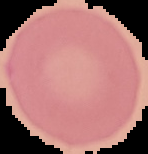
Image is 148×154 pixels. The area outside the segmented cell region is set to black. Result: negative for Plasmodium parasites. From a thin blood smear.